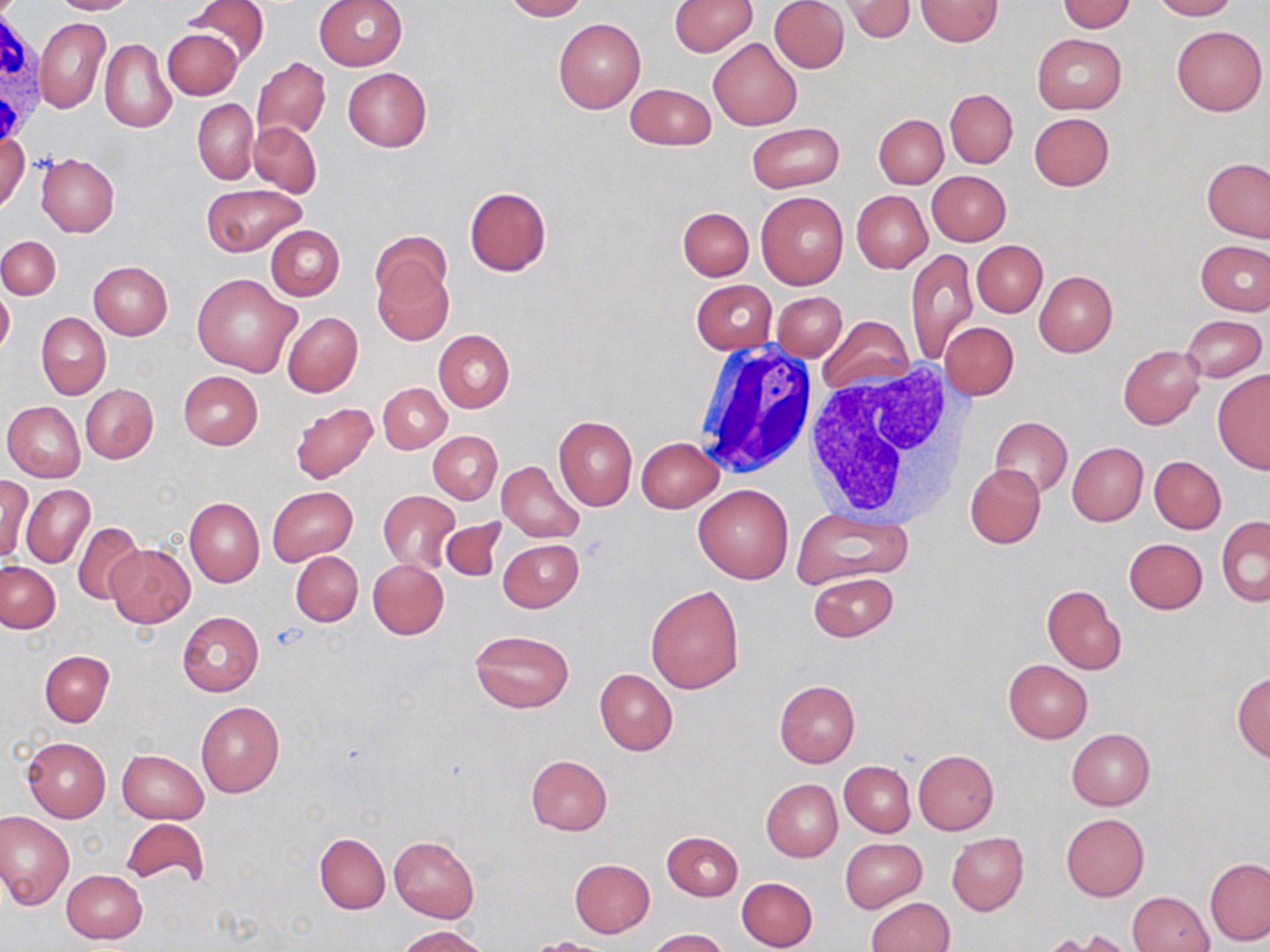

{
  "slide_level_diagnosis": "no evidence of blood parasites",
  "stain": "May-Grünwald-Giemsa",
  "magnification": "1000x",
  "uninfected_red_blood_cell_locations": "approximate bounding boxes as [x1, y1, x2, y2] in pixels: [50, 0, 136, 14], [181, 0, 269, 69], [314, 0, 408, 70], [502, 0, 586, 21], [669, 0, 757, 57], [769, 0, 849, 73], [844, 0, 916, 42], [915, 0, 1002, 46], [1058, 0, 1135, 33], [1151, 0, 1237, 20], [36, 19, 110, 114], [554, 19, 646, 114], [1171, 24, 1267, 116], [163, 26, 242, 100], [1032, 34, 1126, 114], [708, 37, 803, 130], [100, 38, 176, 132], [250, 56, 330, 142], [342, 67, 431, 151], [626, 83, 715, 150], [945, 89, 1017, 168], [193, 98, 258, 184], [1028, 112, 1114, 191], [873, 114, 948, 189], [248, 121, 321, 196], [747, 122, 844, 194], [1, 130, 29, 214], [36, 153, 120, 236], [1201, 158, 1269, 242], [927, 170, 1011, 246], [201, 184, 307, 256], [463, 187, 552, 277], [851, 190, 932, 273], [756, 192, 848, 289], [677, 207, 754, 281], [267, 225, 344, 300], [0, 236, 60, 299], [1195, 239, 1270, 316], [973, 241, 1047, 317], [906, 249, 978, 365], [372, 253, 454, 344], [89, 260, 173, 339], [1034, 271, 1116, 356], [193, 273, 301, 377], [691, 279, 776, 354], [0, 287, 14, 357], [773, 292, 846, 361], [36, 312, 110, 399], [281, 312, 362, 396], [1182, 314, 1267, 382], [819, 315, 914, 397], [941, 322, 1018, 401], [433, 330, 514, 412], [1118, 345, 1205, 429], [1212, 370, 1270, 475], [178, 371, 263, 449], [378, 383, 451, 453], [81, 384, 158, 464], [2, 401, 85, 481], [290, 403, 379, 483], [553, 415, 637, 512], [990, 416, 1073, 496], [428, 431, 501, 504], [636, 437, 723, 512], [1068, 442, 1147, 526], [1150, 456, 1225, 534], [496, 460, 586, 544], [965, 464, 1045, 548], [0, 474, 32, 562], [22, 484, 95, 568], [693, 485, 793, 584], [267, 487, 357, 565], [378, 490, 459, 571], [185, 497, 264, 586], [791, 513, 914, 587], [1216, 517, 1269, 607], [442, 519, 505, 583], [73, 521, 146, 604], [1123, 537, 1207, 614], [498, 539, 583, 613], [107, 543, 196, 628], [291, 551, 363, 626], [369, 559, 448, 639], [1, 561, 60, 632], [809, 572, 898, 641], [645, 585, 744, 693], [1042, 585, 1126, 675], [178, 612, 263, 695], [471, 630, 573, 712], [40, 651, 113, 726], [1003, 659, 1093, 743], [594, 669, 677, 755], [1232, 672, 1270, 763], [774, 680, 860, 768], [195, 701, 284, 798], [1067, 728, 1155, 810], [23, 737, 111, 822], [913, 749, 999, 833], [117, 750, 209, 824], [525, 755, 612, 836], [839, 761, 915, 837], [762, 772, 913, 848], [761, 779, 842, 861], [1, 812, 74, 907], [1060, 813, 1150, 900], [120, 818, 210, 889], [662, 831, 742, 900], [947, 832, 1028, 915], [315, 833, 390, 914], [389, 835, 478, 922], [840, 838, 927, 913], [1205, 857, 1270, 944], [569, 859, 655, 936], [61, 869, 147, 944], [736, 877, 817, 951], [1127, 891, 1214, 952], [865, 897, 953, 952], [397, 925, 489, 952], [645, 928, 729, 952], [531, 936, 610, 952]",
  "image_size": "1270×952 pixels",
  "preparation": "thin blood smear",
  "white_blood_cell_locations": "approximate bounding boxes as [x1, y1, x2, y2] in pixels: [0, 6, 48, 149], [692, 344, 817, 477], [808, 358, 972, 525]",
  "field_of_view": "one of a larger specimen",
  "modality": "optical microscopy"
}